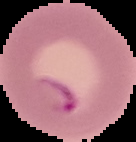
Summary:
  - Malaria status: parasitized
  - Image type: segmented cell region on a black background
  - Image size: 136×142 pixels
  - Preparation: thin blood smear